Report the malaria status of this cell.
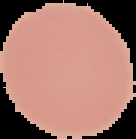
It is uninfected.

From a thin blood film. The area outside the segmented cell region is set to black. Image is 136×139 pixels.